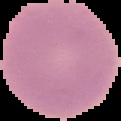
{
  "image_size": "121×121 pixels",
  "preparation": "thin blood film",
  "image_type": "segmented cell region with the area outside set to black",
  "result": "no malaria parasites seen"
}